Name the parasite shown.
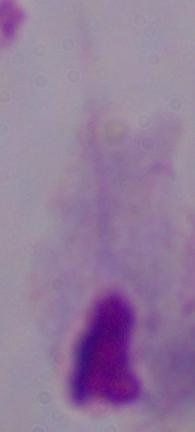

This is a trichomonad.

Summary:
  - Magnification: 1000x
  - Modality: micrograph